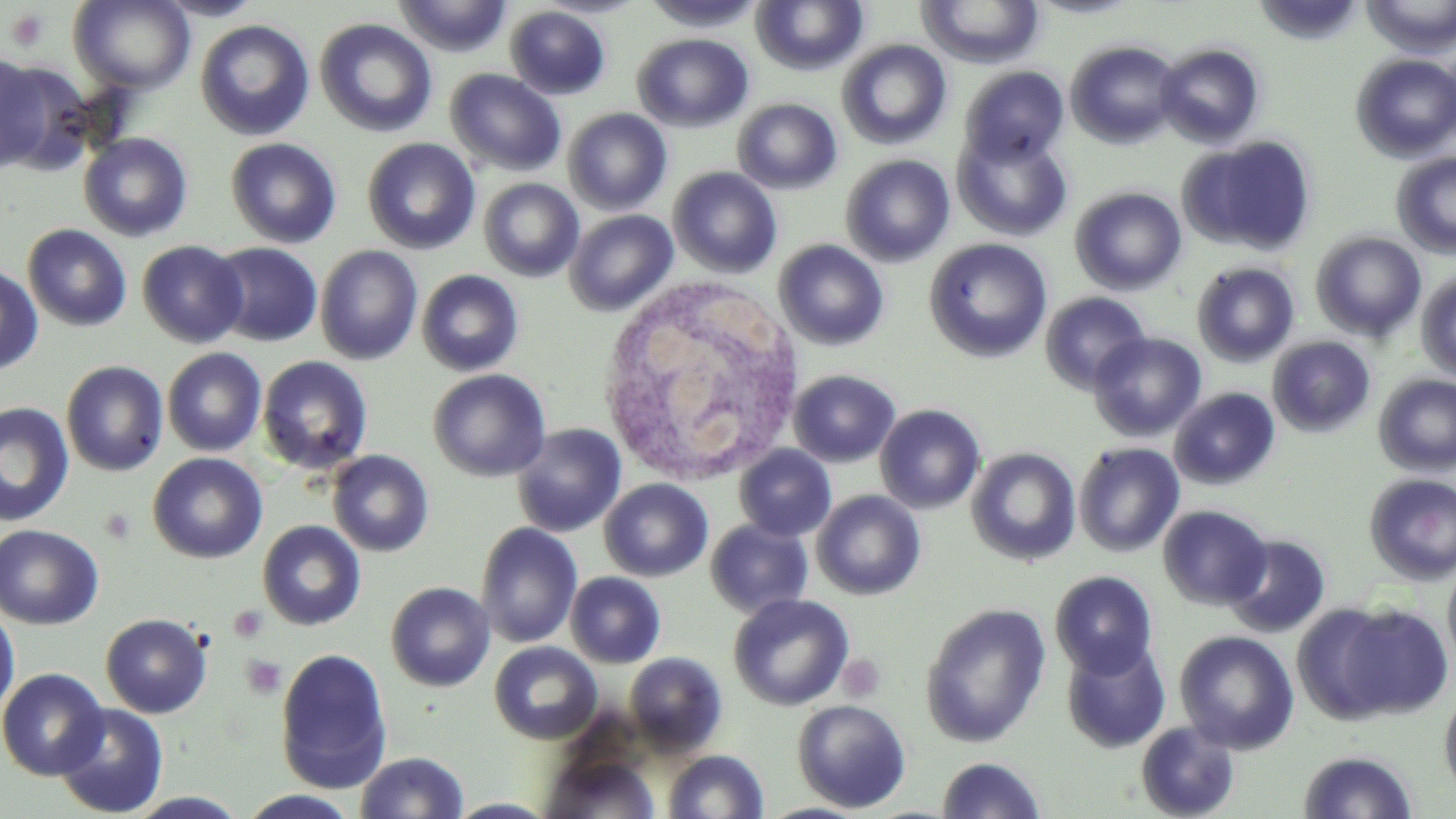

Summary:
  - Coordinate format: approximate bounding boxes as named x1/y1/x2/y2 corners in pixels
  - Uninfected red blood cell locations: (x1=153, y1=0, x2=266, y2=21), (x1=394, y1=0, x2=512, y2=56), (x1=642, y1=0, x2=766, y2=32), (x1=751, y1=0, x2=868, y2=75), (x1=918, y1=0, x2=1045, y2=68), (x1=1252, y1=0, x2=1365, y2=45), (x1=1362, y1=0, x2=1456, y2=58), (x1=69, y1=1, x2=195, y2=93), (x1=505, y1=5, x2=611, y2=100), (x1=314, y1=18, x2=437, y2=137), (x1=195, y1=19, x2=315, y2=141), (x1=632, y1=33, x2=754, y2=132), (x1=837, y1=39, x2=952, y2=149), (x1=1066, y1=40, x2=1183, y2=148), (x1=1155, y1=43, x2=1265, y2=148), (x1=1351, y1=53, x2=1456, y2=162), (x1=0, y1=54, x2=65, y2=174), (x1=959, y1=60, x2=1185, y2=160), (x1=960, y1=66, x2=1069, y2=165), (x1=445, y1=68, x2=566, y2=177), (x1=732, y1=98, x2=842, y2=194), (x1=563, y1=108, x2=672, y2=215), (x1=952, y1=128, x2=1073, y2=241), (x1=78, y1=132, x2=193, y2=242), (x1=1181, y1=136, x2=1317, y2=256), (x1=225, y1=137, x2=342, y2=249), (x1=362, y1=138, x2=480, y2=254), (x1=1392, y1=152, x2=1456, y2=259), (x1=840, y1=154, x2=955, y2=267), (x1=668, y1=167, x2=782, y2=278), (x1=479, y1=178, x2=584, y2=282), (x1=1070, y1=187, x2=1187, y2=295), (x1=564, y1=210, x2=678, y2=316), (x1=22, y1=224, x2=132, y2=331), (x1=1311, y1=231, x2=1426, y2=342), (x1=924, y1=238, x2=1053, y2=363), (x1=774, y1=239, x2=890, y2=351), (x1=137, y1=240, x2=248, y2=347), (x1=208, y1=242, x2=323, y2=346), (x1=315, y1=245, x2=423, y2=365), (x1=1191, y1=262, x2=1300, y2=367), (x1=0, y1=264, x2=44, y2=375), (x1=416, y1=269, x2=524, y2=376), (x1=1416, y1=271, x2=1456, y2=380), (x1=1040, y1=291, x2=1151, y2=393), (x1=1088, y1=331, x2=1206, y2=441), (x1=1268, y1=336, x2=1376, y2=438), (x1=162, y1=347, x2=267, y2=457), (x1=257, y1=356, x2=373, y2=475), (x1=61, y1=360, x2=168, y2=476), (x1=428, y1=368, x2=551, y2=482), (x1=789, y1=369, x2=900, y2=467), (x1=1374, y1=374, x2=1456, y2=476), (x1=1169, y1=387, x2=1280, y2=490), (x1=0, y1=402, x2=74, y2=526), (x1=875, y1=404, x2=985, y2=513), (x1=512, y1=423, x2=626, y2=537), (x1=1074, y1=442, x2=1184, y2=557), (x1=734, y1=444, x2=836, y2=541), (x1=967, y1=447, x2=1081, y2=566), (x1=327, y1=450, x2=434, y2=557), (x1=148, y1=453, x2=267, y2=563), (x1=1364, y1=474, x2=1456, y2=584), (x1=599, y1=478, x2=713, y2=581), (x1=812, y1=490, x2=926, y2=600), (x1=1157, y1=505, x2=1272, y2=610), (x1=706, y1=519, x2=813, y2=618), (x1=257, y1=520, x2=366, y2=631), (x1=475, y1=522, x2=582, y2=648), (x1=0, y1=523, x2=104, y2=629), (x1=1223, y1=534, x2=1331, y2=638), (x1=1443, y1=555, x2=1456, y2=673), (x1=1050, y1=570, x2=1159, y2=677), (x1=565, y1=571, x2=666, y2=668), (x1=386, y1=581, x2=496, y2=691), (x1=728, y1=593, x2=853, y2=710), (x1=1328, y1=602, x2=1453, y2=721), (x1=920, y1=603, x2=1051, y2=747), (x1=0, y1=604, x2=20, y2=721), (x1=100, y1=613, x2=212, y2=718), (x1=1175, y1=630, x2=1299, y2=754), (x1=1061, y1=638, x2=1170, y2=753), (x1=489, y1=641, x2=602, y2=744), (x1=275, y1=648, x2=393, y2=793), (x1=624, y1=651, x2=727, y2=755), (x1=0, y1=668, x2=108, y2=780), (x1=1439, y1=690, x2=1456, y2=797), (x1=792, y1=699, x2=912, y2=813), (x1=53, y1=702, x2=169, y2=818), (x1=1135, y1=721, x2=1240, y2=819), (x1=662, y1=749, x2=769, y2=818), (x1=1298, y1=750, x2=1418, y2=818), (x1=355, y1=751, x2=470, y2=818), (x1=541, y1=754, x2=660, y2=819), (x1=937, y1=757, x2=1045, y2=818), (x1=238, y1=790, x2=361, y2=818), (x1=124, y1=791, x2=251, y2=818), (x1=445, y1=798, x2=560, y2=818)
  - Platelet locations: (x1=4, y1=7, x2=51, y2=52), (x1=99, y1=505, x2=138, y2=544), (x1=228, y1=605, x2=269, y2=643), (x1=240, y1=654, x2=287, y2=699), (x1=837, y1=654, x2=886, y2=702)
  - White blood cell locations: (x1=594, y1=274, x2=809, y2=487)
  - Slide-level diagnosis: no evidence of blood parasites
  - Magnification: 1000x
  - Stain: May-Grünwald-Giemsa
  - Preparation: thin blood film
  - Modality: light microscopy
  - Image size: 1456×819 pixels
  - Field of view: single